Assess this cell for malaria.
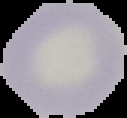
It is uninfected.

Summary:
  - Preparation: thin blood smear
  - Image type: cell region segmented out of the field of view; surrounding area masked to black
  - Image size: 127×118 pixels